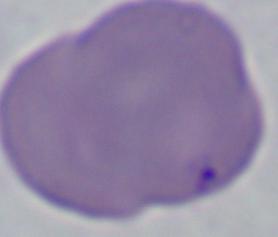

A Babesia parasite is shown. Photomicrograph. 1000x magnification.